Point out each Plasmodium parasite.
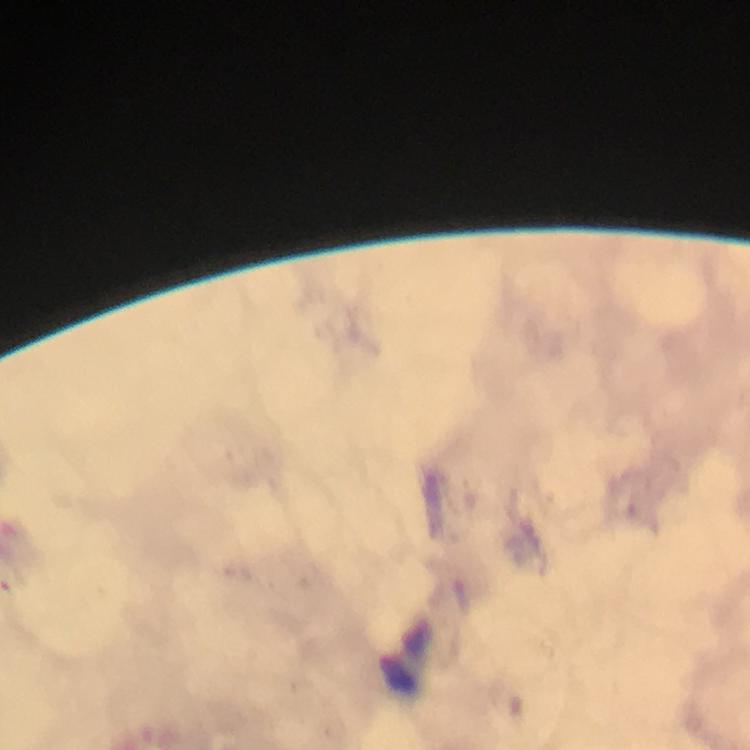
No Plasmodium parasites detected.

Approximate centers as {x, y} in pixels. Leukocyte locations: {404, 658}. From a diagnostic examination for malaria. Giemsa stain. Immersion oil was used. Cropped region of a single field of view. Photographed through the microscope with a smartphone camera. Image is 750×750 pixels. 100x magnification. Thick blood film.